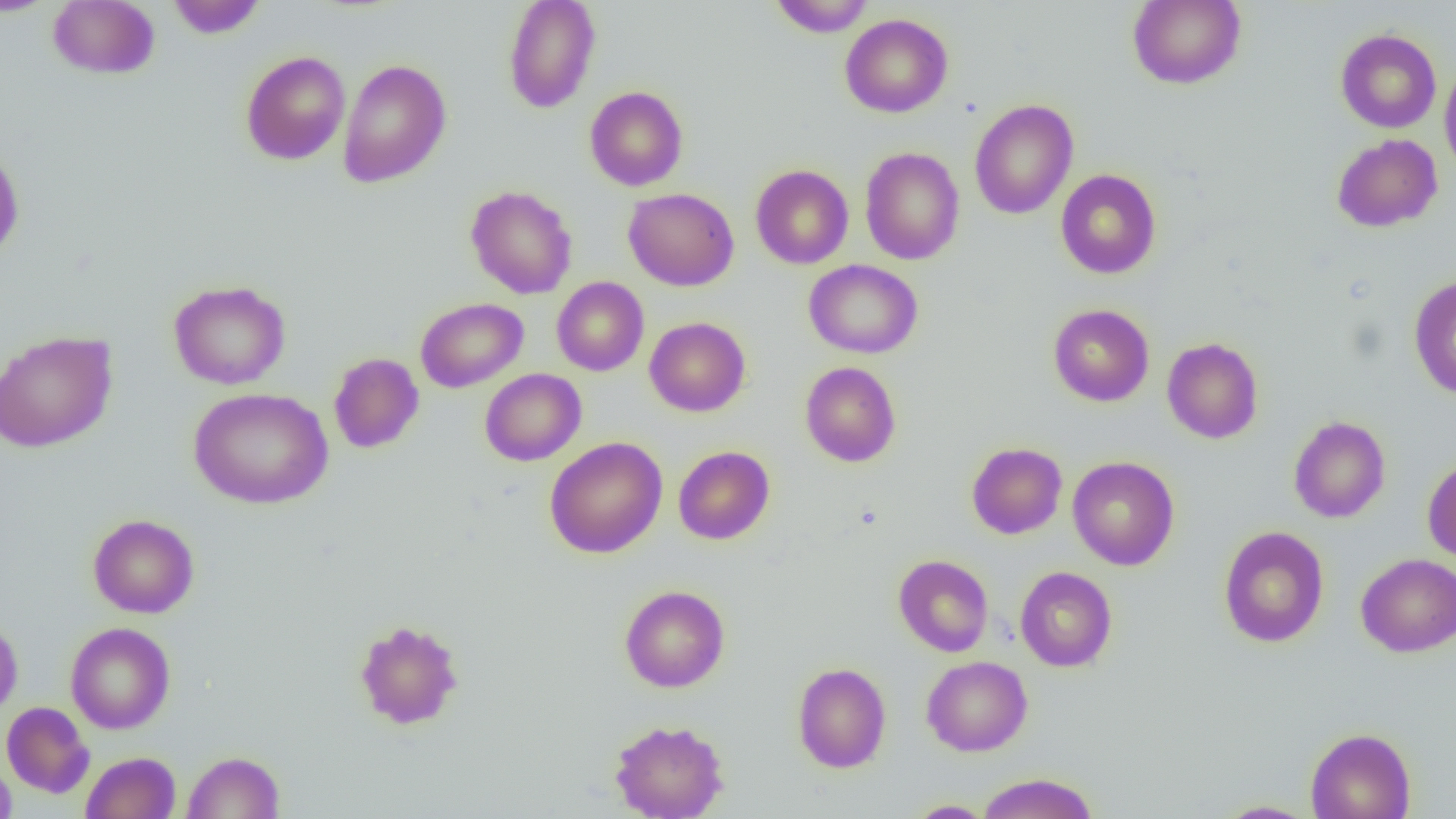

Approximate bounding boxes as (x1,y1)-(x2,y2) corner pairs in pixels. Uninfected red blood cell locations: (0,0)-(58,16), (166,0)-(266,39), (503,0)-(601,114), (769,0)-(875,37), (1128,0)-(1246,89), (48,1)-(160,79), (840,13)-(953,118), (1335,28)-(1441,133), (240,50)-(350,165), (337,59)-(451,188), (1439,59)-(1456,180), (585,86)-(688,190), (969,99)-(1078,220), (1331,133)-(1443,233), (0,142)-(24,262), (860,147)-(965,265), (750,164)-(853,269), (1056,169)-(1161,279), (465,185)-(577,299), (624,188)-(739,291), (804,259)-(923,359), (552,276)-(649,376), (1408,276)-(1456,399), (168,279)-(291,390), (415,298)-(528,392), (1048,304)-(1154,407), (644,316)-(751,416), (0,330)-(117,453), (1162,337)-(1264,444), (328,352)-(424,454), (800,361)-(901,467), (480,368)-(586,466), (187,387)-(334,509), (1288,416)-(1391,523), (544,437)-(667,559), (966,442)-(1067,539), (673,446)-(774,544), (1068,455)-(1179,570), (1422,458)-(1456,564), (88,514)-(199,618), (1218,526)-(1329,647), (1356,553)-(1456,657), (893,554)-(994,657), (1015,566)-(1117,672), (620,585)-(730,693), (0,617)-(23,721), (354,619)-(465,730), (65,621)-(175,734), (921,656)-(1033,756), (792,662)-(891,773), (1,702)-(94,798), (609,719)-(728,819), (1305,727)-(1416,819), (81,751)-(181,819), (182,751)-(285,818), (0,754)-(17,819), (976,772)-(1099,819), (905,800)-(997,818), (1215,800)-(1320,818). Slide-level diagnosis: no evidence of blood parasites. Captured at 1000x magnification. Thin blood smear. Image is 1456×819 pixels. Single field of view. Light microscopy.